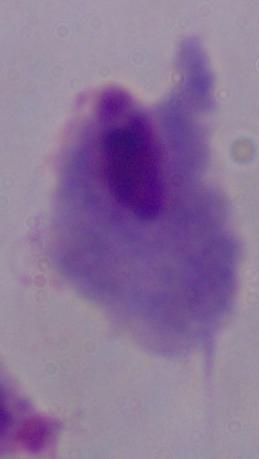 Captured at 1000x magnification. Photomicrograph. A trichomonad is seen.